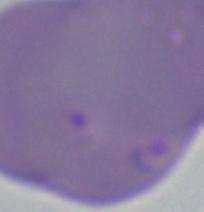

Captured at 1000x magnification. A Babesia parasite is seen. Photomicrograph.